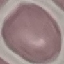
{
  "malaria_status": "uninfected",
  "image_type": "automatically extracted cell patch, resized to 64 × 64 pixels",
  "capture": "smartphone through the microscope eyepiece",
  "stain": "Giemsa",
  "preparation": "thin blood smear"
}